Assess this cell for malaria.
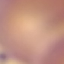
It is uninfected.

Summary:
  - Stain: Giemsa
  - Image type: cell patch, automatically extracted from a larger field of view and resized to 64 × 64 pixels
  - Preparation: thin smear
  - Capture: smartphone camera at the microscope eyepiece